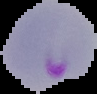

preparation = thin blood film
image type = segmented cell region with the area outside set to black
malaria status = parasitized
image size = 97×94 pixels